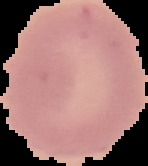 Result: no malaria parasites detected. Segmented cell region on a black background. Image is 148×166 pixels. From a thin blood smear.